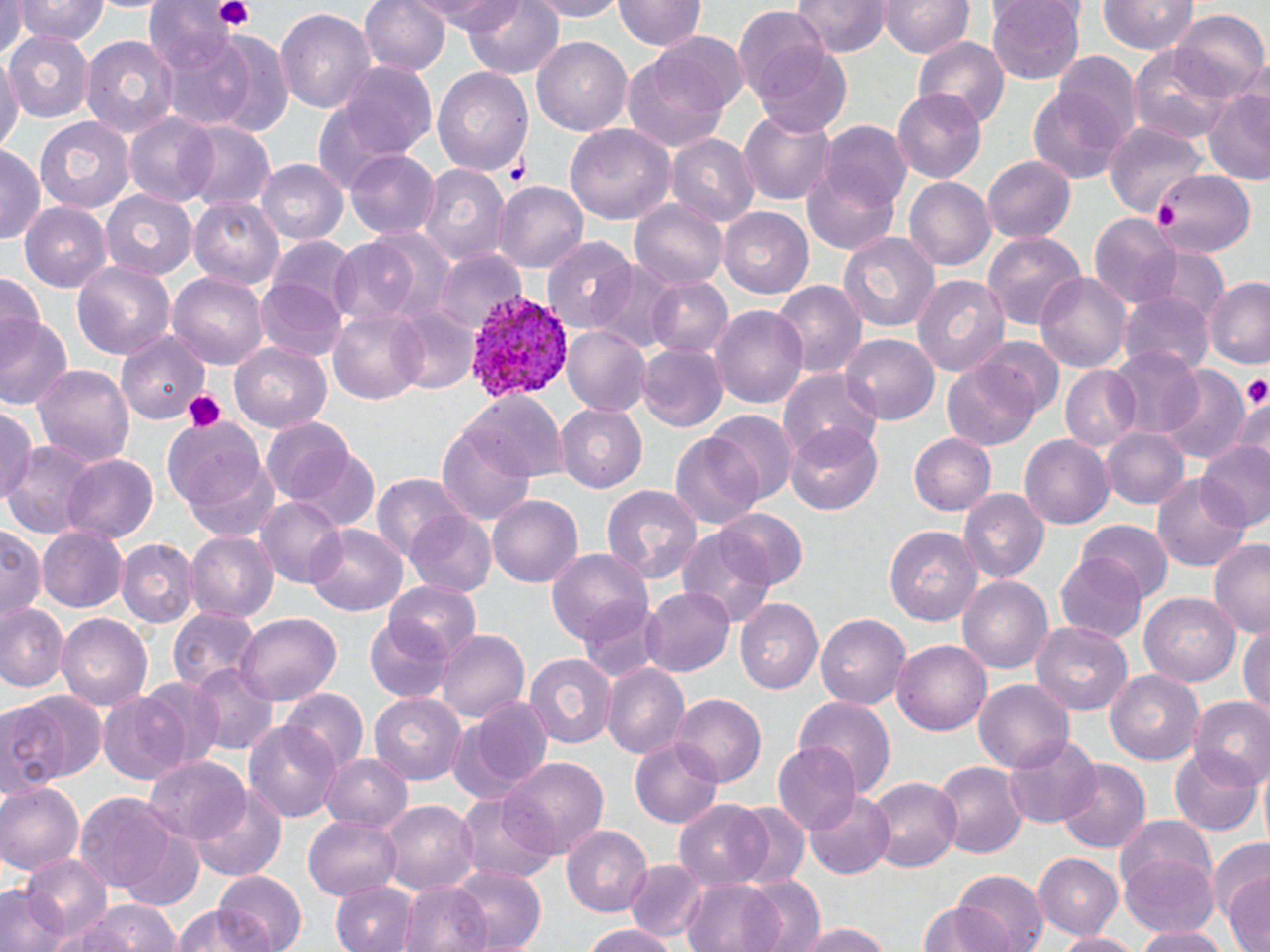 Approximate bounding boxes as [x1, y1, x2, y2] in pixels. Uninfected red blood cell locations: [10, 0, 111, 46], [359, 0, 450, 78], [419, 0, 521, 32], [462, 0, 564, 81], [525, 0, 631, 20], [615, 0, 705, 53], [791, 0, 891, 58], [987, 0, 1085, 85], [1098, 0, 1198, 55], [882, 1, 973, 59], [1, 3, 28, 55], [275, 6, 375, 117], [735, 8, 832, 104], [1170, 9, 1267, 101], [149, 23, 261, 132], [4, 28, 94, 122], [641, 30, 749, 120], [203, 31, 294, 136], [78, 33, 177, 139], [532, 36, 632, 138], [911, 37, 1011, 135], [1129, 43, 1235, 144], [754, 44, 852, 139], [1055, 51, 1139, 143], [0, 52, 20, 161], [623, 53, 733, 153], [340, 61, 438, 160], [433, 68, 534, 178], [1027, 84, 1131, 186], [1204, 87, 1270, 185], [897, 89, 985, 183], [310, 103, 406, 201], [738, 105, 834, 207], [121, 112, 221, 206], [35, 115, 135, 214], [183, 122, 275, 213], [818, 122, 913, 215], [1106, 122, 1209, 213], [565, 124, 675, 224], [667, 135, 759, 227], [0, 144, 45, 244], [345, 151, 438, 241], [983, 157, 1074, 244], [257, 159, 347, 246], [417, 163, 511, 268], [802, 163, 900, 254], [1147, 169, 1253, 258], [901, 176, 994, 271], [492, 178, 592, 274], [101, 191, 197, 280], [189, 196, 286, 289], [629, 199, 728, 290], [20, 202, 111, 292], [720, 207, 813, 299], [1088, 214, 1183, 310], [335, 226, 457, 328], [981, 229, 1087, 334], [836, 231, 941, 335], [543, 236, 635, 331], [267, 238, 358, 323], [1155, 247, 1226, 320], [433, 249, 523, 335], [72, 258, 179, 362], [588, 262, 683, 355], [1035, 270, 1133, 372], [0, 271, 43, 341], [168, 272, 268, 368], [913, 275, 1009, 380], [646, 276, 733, 360], [1203, 277, 1270, 369], [255, 280, 347, 363], [772, 281, 865, 379], [1121, 291, 1214, 379], [393, 304, 481, 394], [712, 305, 808, 409], [329, 307, 430, 404], [0, 314, 72, 411], [563, 326, 650, 415], [116, 328, 208, 424], [840, 332, 939, 425], [976, 337, 1064, 423], [230, 342, 333, 433], [639, 343, 727, 431], [1108, 345, 1204, 440], [943, 358, 1042, 451], [33, 364, 134, 465], [1060, 366, 1141, 450], [1159, 367, 1250, 463], [778, 370, 881, 458], [459, 391, 563, 481], [1235, 391, 1270, 474], [554, 404, 648, 493], [0, 406, 39, 503], [708, 412, 797, 504], [162, 415, 269, 517], [262, 419, 358, 505], [786, 426, 884, 514], [1103, 426, 1189, 511], [436, 429, 536, 525], [909, 431, 994, 515], [670, 433, 764, 530], [1022, 435, 1113, 529], [1196, 440, 1270, 531], [1, 441, 102, 537], [293, 448, 382, 533], [61, 453, 161, 544], [184, 457, 282, 542], [1153, 471, 1250, 571], [373, 472, 461, 565], [601, 483, 703, 584], [960, 489, 1048, 583], [487, 493, 582, 586], [258, 499, 348, 588], [405, 508, 497, 598], [714, 508, 808, 591], [1078, 521, 1170, 606], [306, 522, 407, 618], [883, 524, 983, 626], [1, 525, 46, 623], [676, 525, 777, 629], [39, 526, 127, 610], [187, 532, 277, 622], [118, 540, 198, 626], [1208, 541, 1270, 636], [547, 548, 653, 647], [1055, 551, 1149, 642], [959, 577, 1052, 675], [384, 581, 483, 665], [642, 585, 734, 677], [1140, 591, 1243, 686], [737, 599, 825, 693], [579, 600, 666, 686], [0, 603, 67, 690], [167, 607, 263, 696], [230, 613, 343, 704], [816, 613, 910, 711], [58, 614, 150, 710], [363, 619, 455, 704], [1030, 620, 1135, 713], [1239, 624, 1270, 718], [436, 629, 529, 724], [892, 639, 992, 735], [522, 650, 618, 749], [602, 663, 689, 760], [187, 664, 279, 756], [1105, 668, 1205, 765], [137, 678, 227, 769], [974, 678, 1073, 774], [282, 686, 367, 768], [12, 691, 105, 789], [99, 693, 191, 784], [371, 694, 465, 786], [673, 695, 766, 787], [795, 696, 895, 796], [1189, 696, 1270, 789], [450, 701, 551, 800], [0, 704, 64, 799], [648, 713, 753, 814], [247, 718, 340, 823], [1004, 732, 1102, 826], [631, 737, 723, 827], [772, 742, 861, 834], [1170, 749, 1262, 835], [321, 751, 413, 832], [505, 755, 608, 856], [143, 757, 250, 847], [1053, 758, 1152, 855], [932, 759, 1027, 857], [865, 774, 961, 869], [0, 780, 83, 875], [193, 785, 287, 879], [454, 791, 556, 887], [803, 791, 896, 878], [75, 793, 176, 893], [675, 801, 773, 888], [381, 802, 478, 890], [727, 802, 810, 888], [1115, 814, 1219, 896], [304, 815, 401, 901], [562, 825, 654, 917], [120, 829, 205, 912], [1205, 837, 1270, 934], [1119, 851, 1221, 938], [1034, 852, 1124, 940], [22, 855, 114, 941], [625, 859, 706, 942], [449, 865, 545, 952], [952, 871, 1045, 952], [1223, 871, 1269, 952], [214, 872, 308, 951], [741, 875, 826, 952], [681, 878, 787, 952], [0, 880, 73, 952], [330, 880, 419, 952], [400, 880, 493, 952], [76, 899, 179, 952], [913, 900, 1019, 952], [168, 906, 272, 952], [785, 921, 894, 952], [580, 922, 681, 952], [1131, 926, 1236, 952], [1056, 929, 1138, 952]. Plasmodium vivax-infected red blood cell locations: [466, 292, 575, 404]. Platelet locations: [212, 0, 255, 32], [501, 155, 532, 186], [1155, 199, 1178, 233], [1245, 374, 1269, 410], [178, 386, 226, 432]. Slide-level diagnosis: Plasmodium vivax. Thin blood smear. 1000x magnification. Light microscopy. One field of a larger specimen. Image is 1270×952 pixels. May-Grünwald-Giemsa-stained preparation.